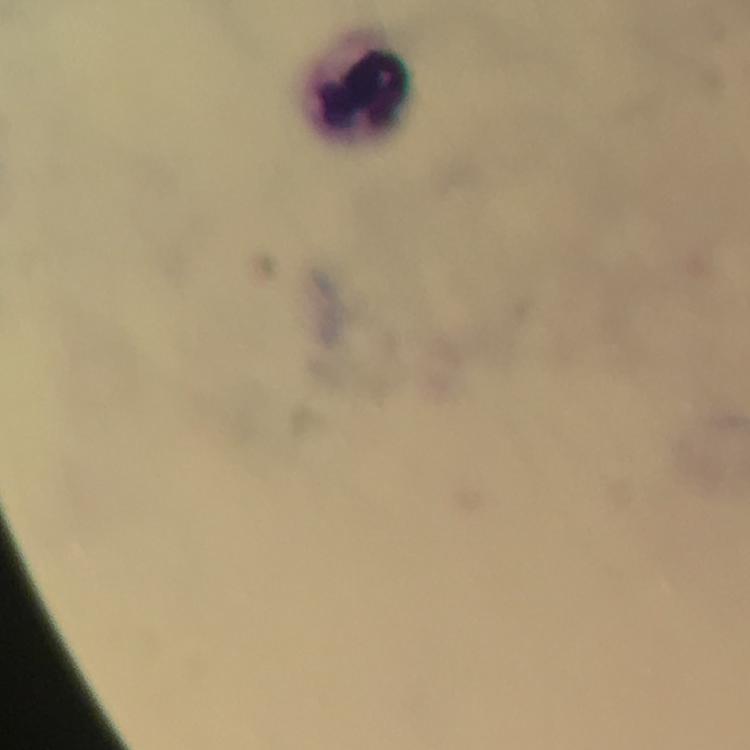
Approximate centers as {x, y} in pixels.
Summary:
  - Leukocyte locations: {365, 90}
  - Magnification: 100x
  - Cropped from: one field of view
  - Immersion oil: applied
  - Context: from a malaria diagnostic workup
  - Preparation: thick blood smear
  - Capture: smartphone camera through the microscope
  - Plasmodium parasites: none detected
  - Stain: Giemsa
  - Image size: 750×750 pixels